Point out each malaria parasite.
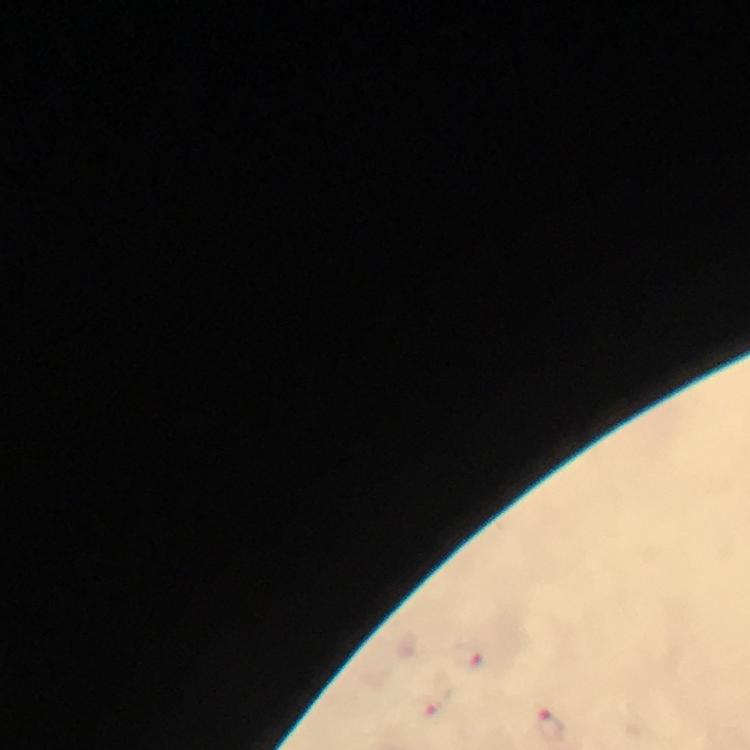
Approximate centers as [x, y] in pixels.
Malaria parasites: [467, 657], [434, 699], [550, 727].

Summary:
  - Stain: Giemsa
  - Context: from a diagnostic examination for malaria
  - Cropped from: a single field of view
  - Capture: smartphone camera through the microscope
  - Immersion oil: applied
  - Magnification: 100x
  - Preparation: thick blood smear
  - Image size: 750×750 pixels